Classify this cell by malaria status.
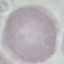
It is uninfected.

Summary:
  - Image type: cell patch, automatically extracted from a larger field of view and resized to 64 × 64 pixels
  - Preparation: thin blood smear
  - Capture: smartphone camera at the microscope eyepiece
  - Stain: Giemsa